Describe the morphology of the red blood cells.
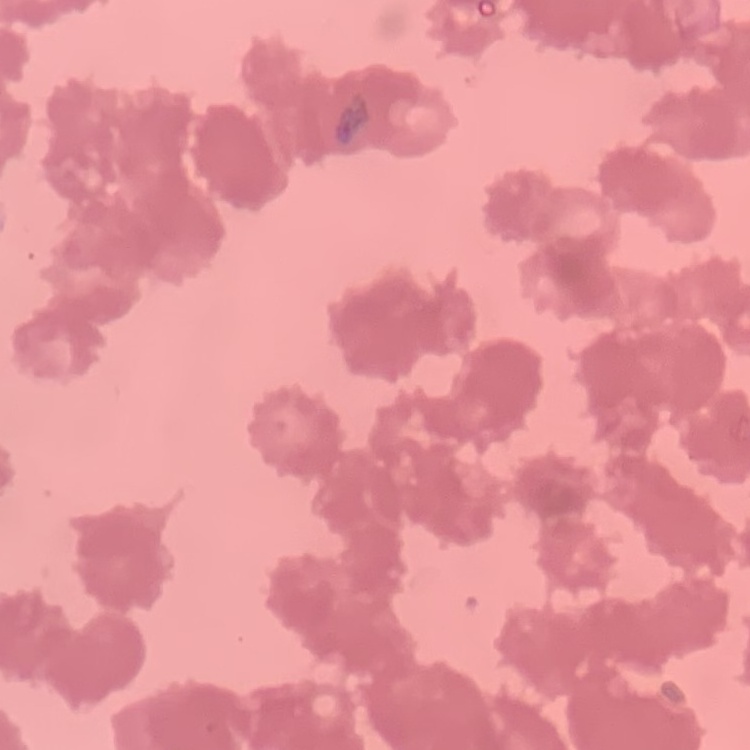
They show rouleaux formation.

Summary:
  - Image type: square crop of a larger photomicrograph
  - Preparation: thin peripheral smear
  - Stain: Field's or Giemsa